Locate every malaria parasite.
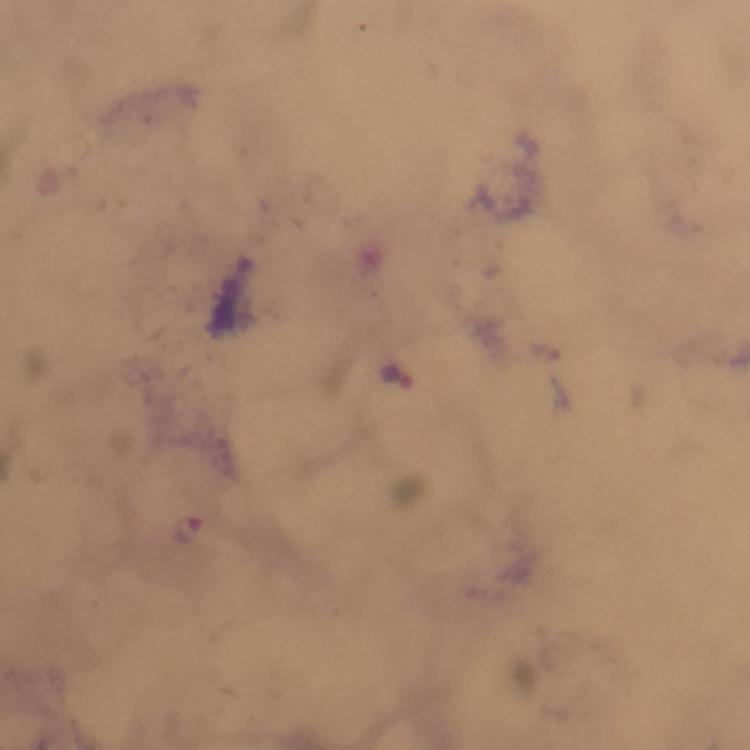
Approximate centers as [x, y] in pixels.
Malaria parasites: [401, 377], [190, 530].

Giemsa-stained preparation. Thick blood film. Smartphone photograph taken through a microscope. Image is 750×750 pixels. Cropped region of a single field of view. 100x magnification. Immersion oil was used. From a malaria diagnostic workup.